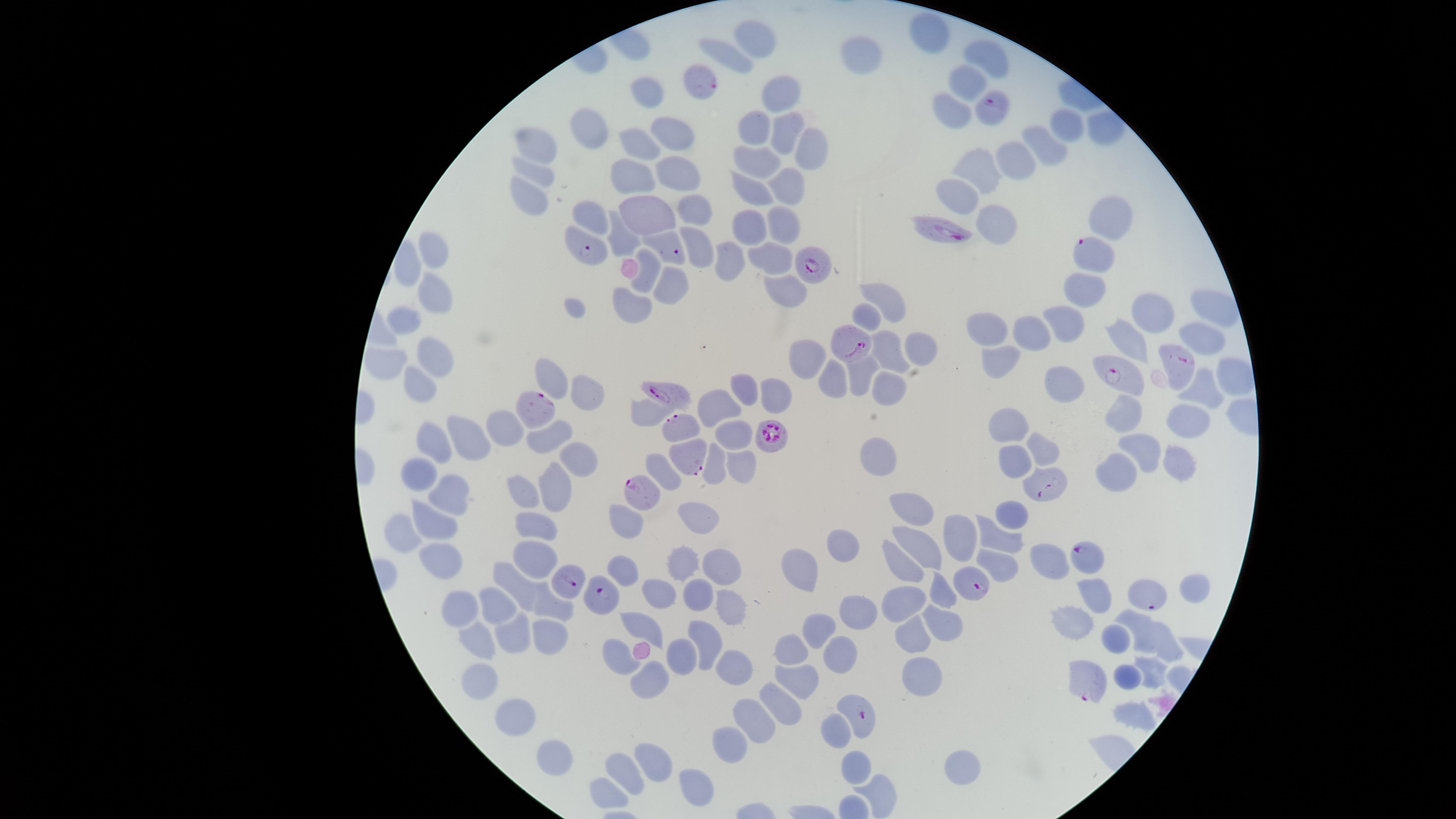
stain = Giemsa
presence = malaria parasites identified
preparation = thin smear of blood
uninfected RBCs = approximate marker points as {x, y} in pixels: {930, 33}, {756, 38}, {858, 55}, {724, 57}, {990, 57}, {966, 87}, {782, 93}, {649, 94}, {949, 112}, {1067, 123}, {759, 128}, {596, 131}, {782, 132}, {670, 136}, {536, 141}, {638, 141}, {1047, 144}, {808, 147}, {1013, 158}, {759, 162}, {980, 170}, {538, 171}, {636, 172}, {682, 176}, {748, 186}, {786, 188}, {960, 196}, {530, 197}, {595, 210}, {653, 211}, {699, 212}, {780, 218}, {1112, 219}, {990, 220}, {750, 222}, {624, 239}, {701, 247}, {769, 253}, {433, 254}, {729, 255}, {651, 272}, {669, 287}, {785, 287}, {1083, 288}, {435, 298}, {890, 299}, {631, 303}, {1209, 311}, {1157, 314}, {869, 315}, {1065, 315}, {407, 322}, {1033, 330}, {991, 331}, {1203, 338}, {1128, 339}, {918, 348}, {891, 353}, {437, 358}, {809, 359}, {385, 362}, {1001, 362}, {858, 368}, {1236, 375}, {552, 378}, {828, 381}, {1071, 382}, {740, 384}, {422, 385}, {775, 388}, {882, 390}, {1202, 390}, {588, 392}, {715, 406}, {646, 411}, {1126, 416}, {1187, 416}, {502, 426}, {1011, 426}, {553, 429}, {732, 432}, {466, 439}, {429, 440}, {1139, 441}, {1038, 448}, {880, 457}, {1010, 458}, {1175, 459}, {571, 464}, {713, 467}, {740, 468}, {1122, 468}, {661, 469}, {419, 477}, {554, 488}, {522, 493}, {449, 494}, {914, 502}, {1012, 512}, {693, 517}, {428, 521}, {624, 521}, {540, 526}, {405, 530}, {954, 534}, {1001, 538}, {924, 540}, {840, 545}, {534, 556}, {1045, 558}, {445, 560}, {682, 561}, {899, 565}, {721, 566}, {995, 568}, {621, 570}, {801, 573}, {514, 583}, {659, 589}, {942, 589}, {697, 593}, {1087, 594}, {1187, 594}, {551, 602}, {730, 604}, {906, 604}, {464, 606}, {495, 611}, {857, 616}, {941, 619}, {1138, 621}, {642, 627}, {1071, 627}, {821, 631}, {479, 634}, {515, 634}, {547, 635}, {1119, 639}, {703, 641}, {916, 641}, {1169, 643}, {792, 650}, {621, 652}, {842, 653}, {679, 656}, {733, 666}, {924, 672}, {1152, 672}, {481, 674}, {1128, 674}, {648, 679}, {803, 680}, {782, 706}, {1133, 711}, {758, 717}, {515, 718}, {834, 732}, {727, 746}, {552, 756}, {655, 761}, {964, 766}, {856, 769}, {621, 770}, {696, 780}, {611, 792}, {885, 794}
species = Plasmodium falciparum
capture = smartphone photograph through the microscope eyepiece
visible region = circular
field of view = single
image size = 1456×819 pixels
parasitized RBCs = approximate marker points as {x, y} in pixels: {699, 79}, {993, 111}, {944, 231}, {672, 248}, {586, 250}, {1090, 254}, {807, 269}, {849, 345}, {1174, 363}, {1119, 377}, {673, 395}, {538, 407}, {679, 426}, {767, 434}, {688, 457}, {1042, 486}, {645, 488}, {1086, 558}, {572, 577}, {976, 585}, {1147, 594}, {604, 600}, {1086, 679}, {863, 715}